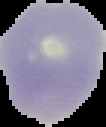

result = negative for malaria parasites
image size = 106×127 pixels
preparation = thin blood smear
image type = cell region segmented out of the field of view; surrounding area masked to black